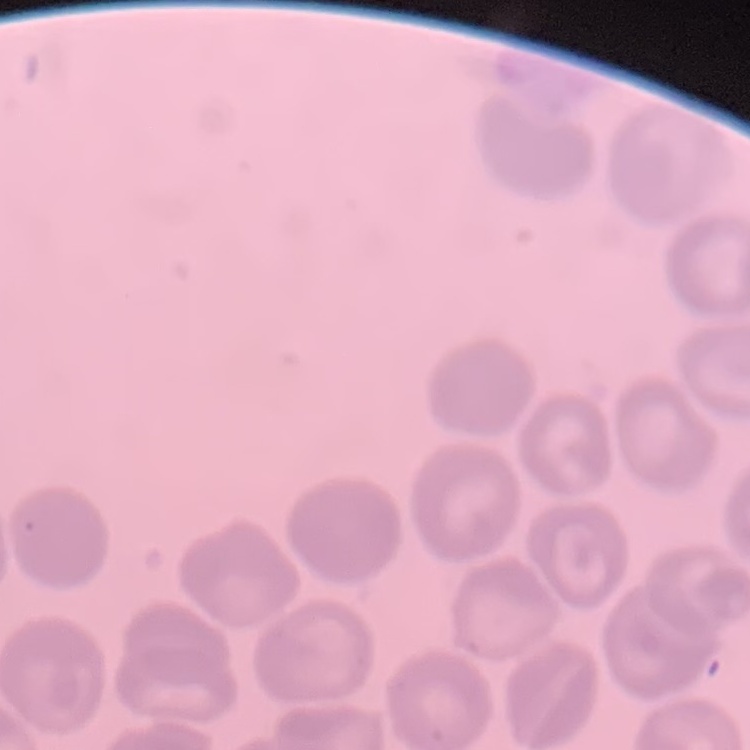
red blood cell morphology = no rouleaux formation
preparation = thin peripheral smear
stain = Field's or Giemsa
image type = square crop of a larger photomicrograph